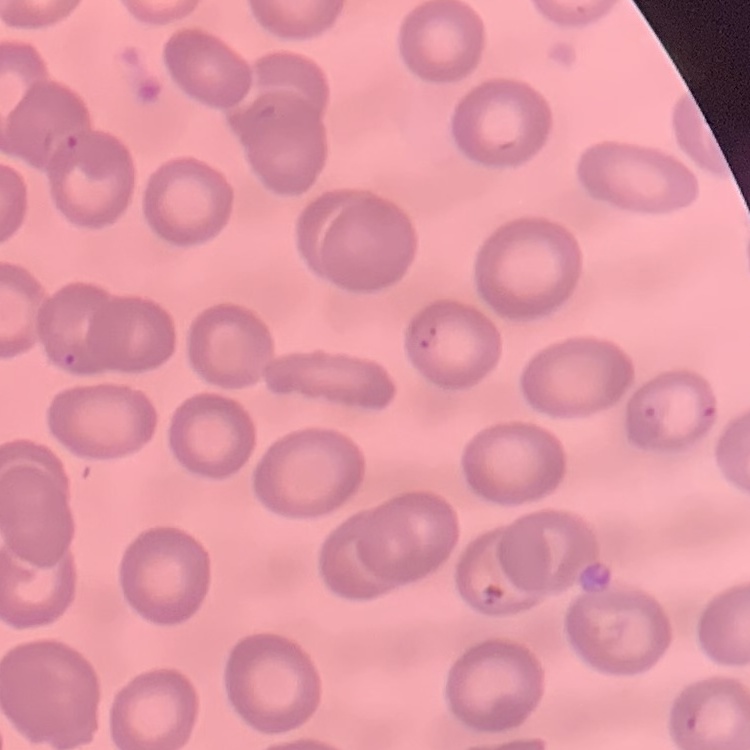
{
  "erythrocyte_morphology": "no rouleaux formation",
  "stain": "Field's or Giemsa",
  "preparation": "thin blood film",
  "image_type": "square crop of a larger photomicrograph"
}